Classify this cell by malaria status.
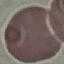

Uninfected.

Giemsa stain. Automatically extracted cell patch, resized to 64 × 64 pixels. Thin blood smear. Acquired by smartphone through the microscope eyepiece.